Locate and identify every blood parasite.
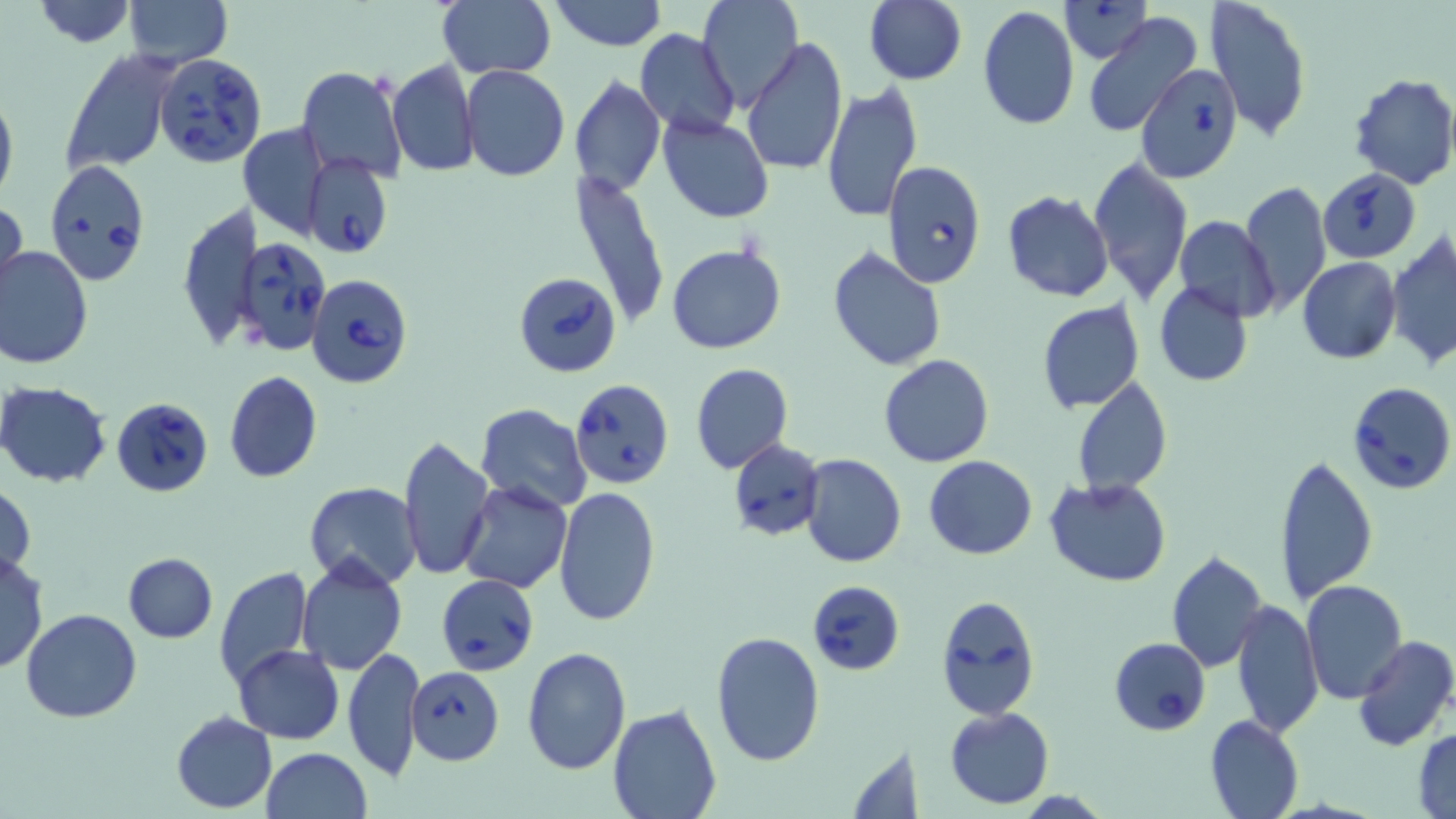
Approximate bounding boxes as (x1,y1)-(x2,y2) corner pairs in pixels.
Babesia divergens-infected red blood cells: (153,53)-(267,166), (1137,66)-(1240,182), (303,154)-(391,260), (43,160)-(151,285), (882,161)-(986,290), (1318,168)-(1421,261), (235,235)-(331,354), (514,270)-(621,378), (306,274)-(413,388), (570,378)-(673,490), (1344,383)-(1454,497), (113,397)-(214,499), (728,437)-(825,540), (436,575)-(538,675), (808,579)-(907,675), (936,595)-(1040,721), (1109,637)-(1212,735), (406,667)-(505,765).
No Plasmodium falciparum, Plasmodium ovale, Plasmodium malariae, Plasmodium vivax, or Trypanosoma brucei observed.

slide_level_diagnosis: Babesia divergens
stain: May-Grünwald-Giemsa
preparation: thin blood smear
uninfected_red_blood_cell_locations: 'approximate bounding boxes as (x1,y1)-(x2,y2) corner pairs in pixels: (28,0)-(140,48), (122,0)-(232,68), (436,0)-(555,79), (550,0)-(666,51), (697,0)-(803,112), (1206,0)-(1312,142), (863,1)-(967,84), (1061,1)-(1151,63), (976,7)-(1079,130), (1083,12)-(1203,139), (634,29)-(740,138), (741,36)-(849,177), (59,49)-(178,175), (387,59)-(478,177), (297,66)-(407,183), (461,66)-(569,182), (1347,72)-(1456,191), (569,75)-(666,196), (821,83)-(922,221), (0,85)-(18,210), (658,115)-(774,223), (238,122)-(330,239), (1086,156)-(1193,304), (568,168)-(673,333), (1239,181)-(1331,317), (1002,190)-(1114,303), (1,197)-(26,307), (178,204)-(260,352), (1174,215)-(1278,322), (1385,232)-(1456,369), (667,244)-(787,354), (0,246)-(94,369), (827,247)-(946,370), (1298,257)-(1401,364), (1155,281)-(1253,387), (1037,300)-(1145,412), (1051,327)-(1161,468), (879,354)-(994,468), (690,363)-(793,474), (224,371)-(323,484), (1070,378)-(1174,497), (1,381)-(114,487), (476,403)-(592,512), (397,433)-(494,581), (1274,450)-(1379,606), (801,454)-(907,568), (924,455)-(1036,559), (1045,477)-(1172,587), (304,481)-(423,590), (460,482)-(572,594), (1,483)-(36,580), (554,488)-(660,628), (1166,549)-(1269,672), (0,552)-(48,673), (122,553)-(217,643), (295,558)-(408,675), (214,567)-(313,691), (1300,579)-(1407,701), (1232,598)-(1322,740), (22,609)-(142,724), (710,631)-(825,767), (1353,636)-(1456,753), (232,645)-(344,744), (342,646)-(424,782), (521,646)-(632,775), (607,703)-(722,818), (945,706)-(1054,809), (170,712)-(277,813), (1204,714)-(1304,819), (1412,728)-(1456,818), (845,742)-(927,818), (260,748)-(372,819)'
modality: light microscopy
image_size: 1456×819 pixels
magnification: 1000x
field_of_view: single